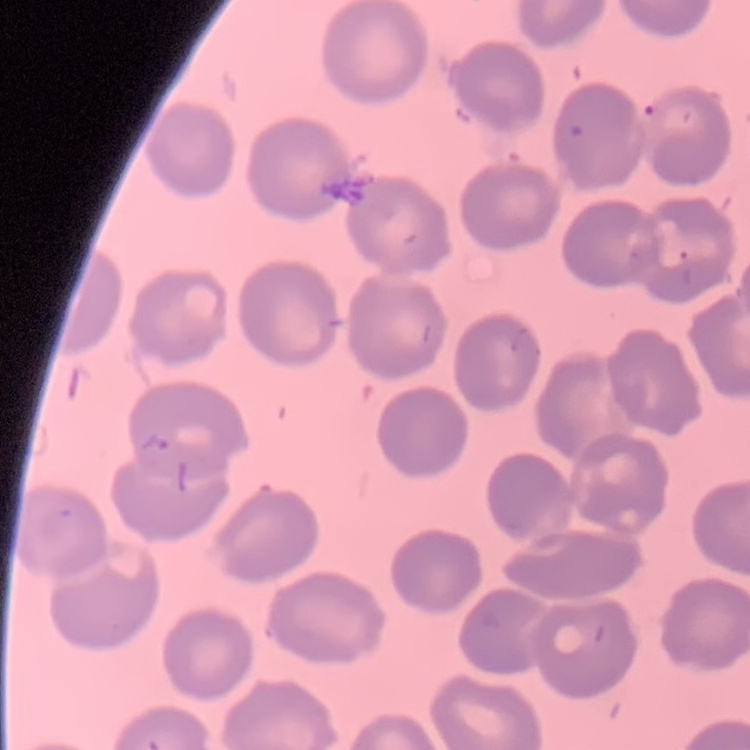
Summary:
  - Red blood cell morphology: no rouleaux formation
  - Preparation: thin peripheral smear
  - Image type: square crop of a larger photomicrograph
  - Stain: Field's or Giemsa